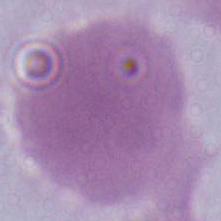

identification = erythrocyte
modality = photomicrograph
magnification = 1000x